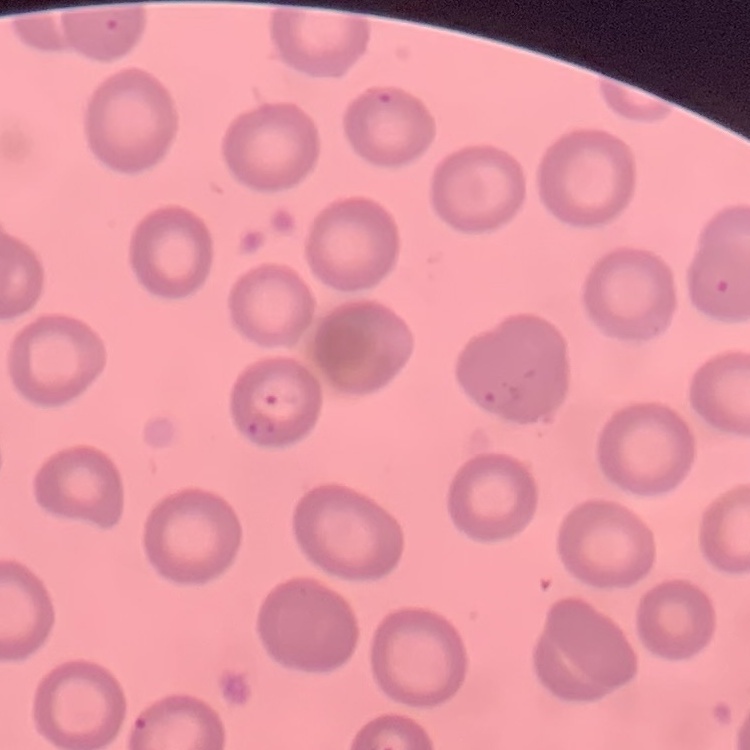
The erythrocytes show no rouleaux formation. One tile cut from a larger photomicrograph. Stained with either Field's or Giemsa. Thin blood film.